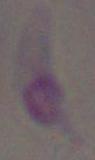

identification = Toxoplasma gondii
modality = micrograph
magnification = 1000x